Name the blood parasite species.
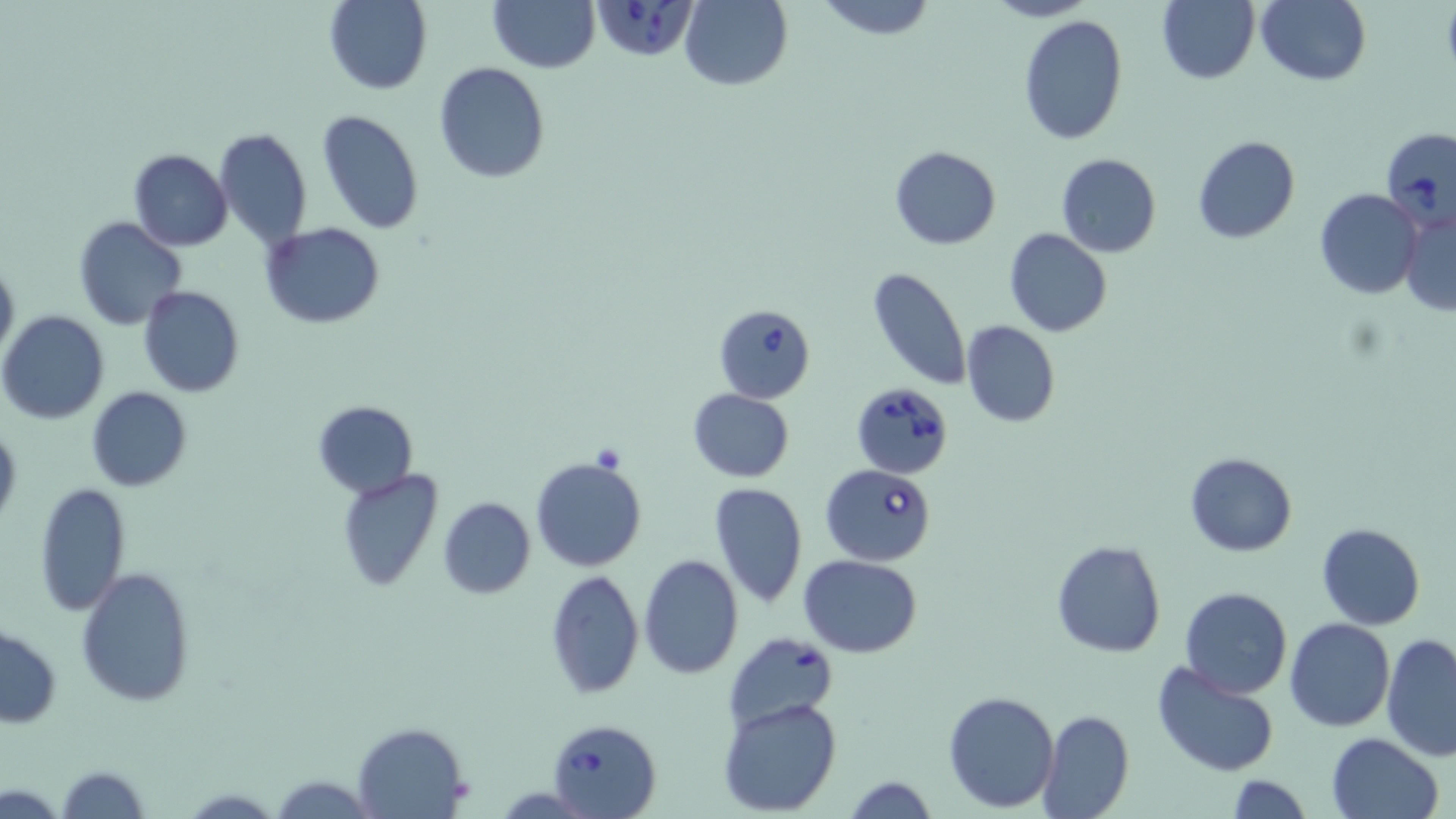

Babesia divergens.

Summary:
  - Coordinate format: approximate bounding boxes as [x1, y1, x2, y2] in pixels
  - Babesia divergens-infected red blood cell locations: [590, 0, 699, 64], [1380, 126, 1454, 227], [712, 303, 817, 403], [850, 380, 955, 479], [822, 464, 939, 564], [724, 633, 836, 732], [548, 719, 663, 818]
  - Uninfected red blood cell locations: [324, 0, 432, 94], [487, 0, 599, 73], [681, 0, 792, 91], [812, 0, 938, 39], [983, 0, 1097, 23], [1158, 0, 1260, 85], [1258, 0, 1371, 86], [1017, 16, 1128, 144], [434, 61, 550, 183], [317, 110, 424, 233], [215, 126, 312, 249], [1192, 136, 1300, 243], [888, 145, 1001, 249], [128, 149, 233, 251], [1055, 152, 1162, 258], [1314, 188, 1423, 299], [1398, 209, 1456, 316], [75, 217, 187, 331], [259, 221, 386, 329], [1004, 228, 1112, 337], [0, 257, 18, 364], [867, 265, 972, 391], [138, 286, 245, 398], [1, 311, 110, 423], [961, 321, 1059, 427], [87, 386, 191, 492], [688, 389, 794, 483], [312, 400, 417, 498], [0, 421, 21, 531], [1185, 452, 1296, 557], [532, 455, 647, 572], [336, 469, 444, 592], [707, 481, 808, 608], [35, 482, 131, 615], [437, 496, 535, 598], [1316, 521, 1425, 631], [1050, 539, 1166, 658], [639, 553, 744, 679], [798, 555, 923, 657], [76, 567, 195, 706], [545, 570, 644, 698], [1179, 587, 1291, 698], [1285, 617, 1395, 731], [0, 626, 62, 729], [1381, 632, 1456, 761], [1153, 661, 1278, 776], [942, 689, 1061, 813], [719, 698, 843, 816], [1036, 709, 1134, 819], [352, 722, 470, 818], [1324, 731, 1445, 819], [57, 766, 149, 819], [269, 773, 373, 816], [842, 774, 940, 819], [1223, 774, 1314, 818]
  - Modality: optical microscopy
  - Preparation: thin blood smear
  - Field of view: one of a larger specimen
  - Image size: 1456×819 pixels
  - Stain: May-Grünwald-Giemsa
  - Magnification: 1000x